Give the extent of all Plasmodium vivax-infected red blood cells.
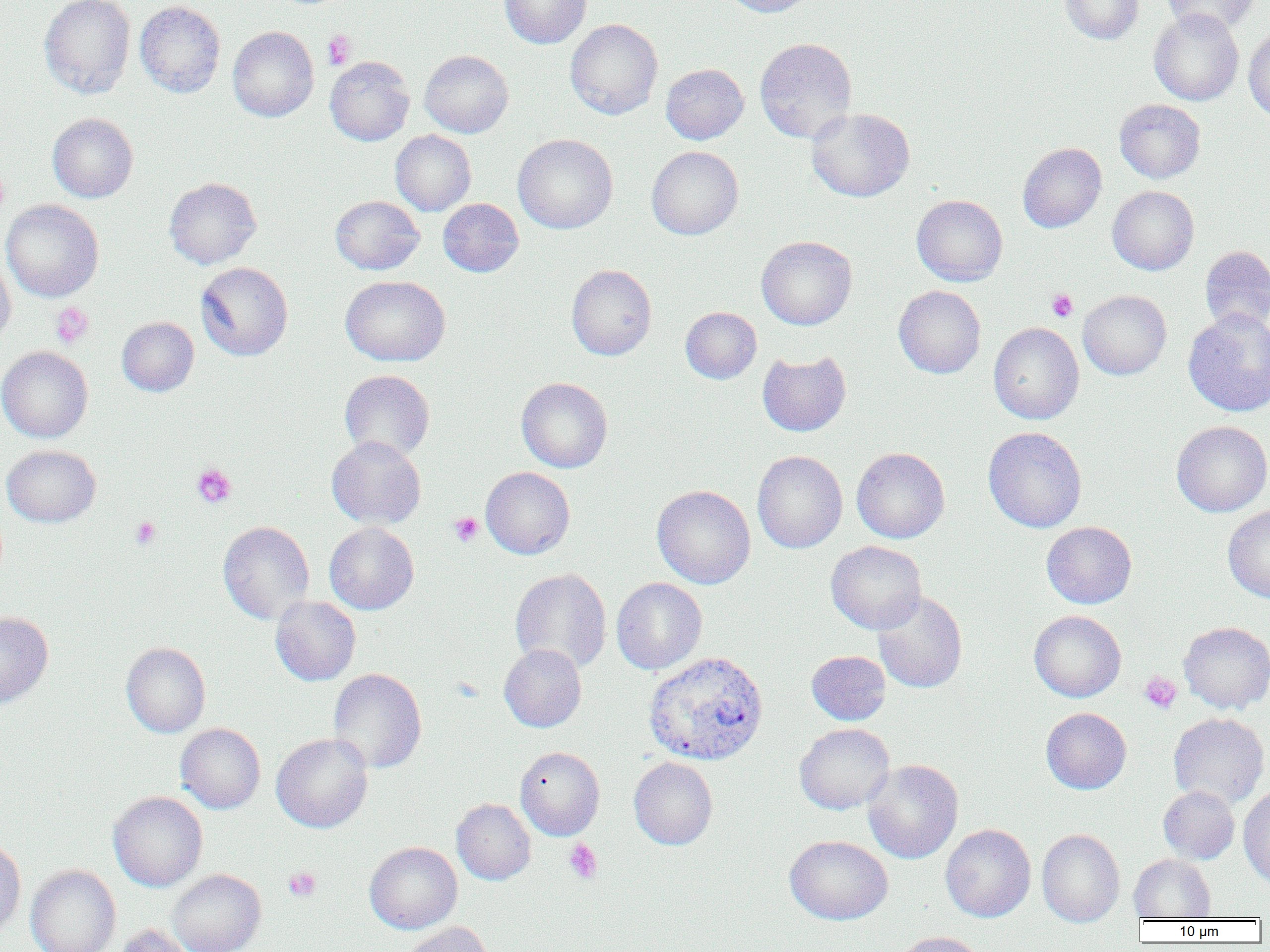
Approximate bounding boxes as [x1, y1, x2, y2] in pixels.
Plasmodium vivax-infected red blood cells: [643, 651, 769, 766].

{
  "slide_level_diagnosis": "Plasmodium vivax",
  "magnification": "1000x",
  "uninfected_red_blood_cell_locations": "approximate bounding boxes as [x1, y1, x2, y2] in pixels: [39, 0, 136, 99], [499, 0, 591, 48], [719, 0, 817, 17], [1059, 0, 1144, 44], [1161, 0, 1261, 35], [134, 1, 225, 98], [1148, 9, 1244, 105], [565, 18, 663, 119], [227, 26, 318, 122], [1243, 26, 1270, 122], [755, 38, 857, 142], [419, 50, 513, 138], [325, 56, 414, 146], [661, 63, 749, 144], [1114, 99, 1205, 183], [806, 107, 915, 202], [47, 113, 138, 202], [390, 130, 476, 216], [513, 134, 618, 234], [1018, 143, 1106, 232], [646, 146, 743, 239], [164, 177, 262, 269], [1107, 186, 1199, 275], [912, 194, 1007, 286], [330, 195, 424, 275], [438, 198, 523, 277], [1, 199, 104, 302], [756, 236, 857, 330], [1200, 246, 1270, 333], [0, 250, 16, 346], [195, 262, 293, 361], [566, 264, 657, 360], [340, 276, 450, 366], [894, 285, 986, 378], [1077, 290, 1171, 380], [680, 307, 761, 383], [1183, 308, 1270, 416], [117, 317, 199, 396], [988, 322, 1084, 424], [0, 346, 93, 442], [757, 350, 851, 436], [339, 370, 435, 462], [516, 377, 613, 473], [1171, 420, 1270, 517], [983, 426, 1087, 532], [327, 436, 426, 529], [1, 444, 101, 527], [851, 447, 950, 543], [752, 450, 848, 553], [480, 467, 575, 559], [652, 485, 755, 589], [1222, 504, 1270, 603], [217, 521, 315, 624], [1041, 521, 1137, 609], [324, 522, 419, 614], [826, 541, 927, 634], [510, 569, 611, 674], [611, 577, 707, 674], [872, 590, 968, 693], [270, 595, 361, 685], [1029, 610, 1126, 702], [0, 611, 53, 710], [1179, 621, 1270, 714], [121, 642, 211, 738], [499, 644, 586, 732], [806, 650, 890, 725], [328, 668, 426, 773], [1041, 707, 1131, 794], [1168, 712, 1269, 809], [175, 723, 266, 814], [794, 723, 895, 814], [271, 733, 373, 833], [515, 746, 605, 840], [629, 756, 718, 849], [862, 759, 964, 864], [1158, 785, 1240, 864], [1238, 788, 1270, 888], [108, 791, 208, 891], [451, 798, 536, 885], [940, 824, 1036, 922], [1037, 829, 1125, 927], [784, 835, 893, 925], [0, 838, 26, 937], [364, 842, 462, 934], [1129, 854, 1215, 920], [25, 864, 121, 952], [168, 869, 266, 952], [402, 922, 493, 952], [109, 924, 196, 952], [891, 932, 986, 952]",
  "field_of_view": "one of a larger specimen",
  "platelet_locations": "approximate bounding boxes as [x1, y1, x2, y2] in pixels: [322, 30, 356, 69], [1047, 289, 1078, 322], [50, 302, 94, 348], [191, 463, 237, 508], [449, 512, 483, 546], [131, 516, 161, 550], [1140, 671, 1181, 713], [564, 839, 603, 884], [283, 866, 321, 902]",
  "preparation": "thin blood smear",
  "modality": "optical microscopy",
  "image_size": "1270×952 pixels"
}